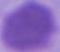

identification: red blood cell
magnification: 1000x
modality: photomicrograph